Identify the parasite.
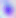

This is Toxoplasma gondii.

Summary:
  - Magnification: 400x
  - Modality: micrograph